Point out each malaria parasite.
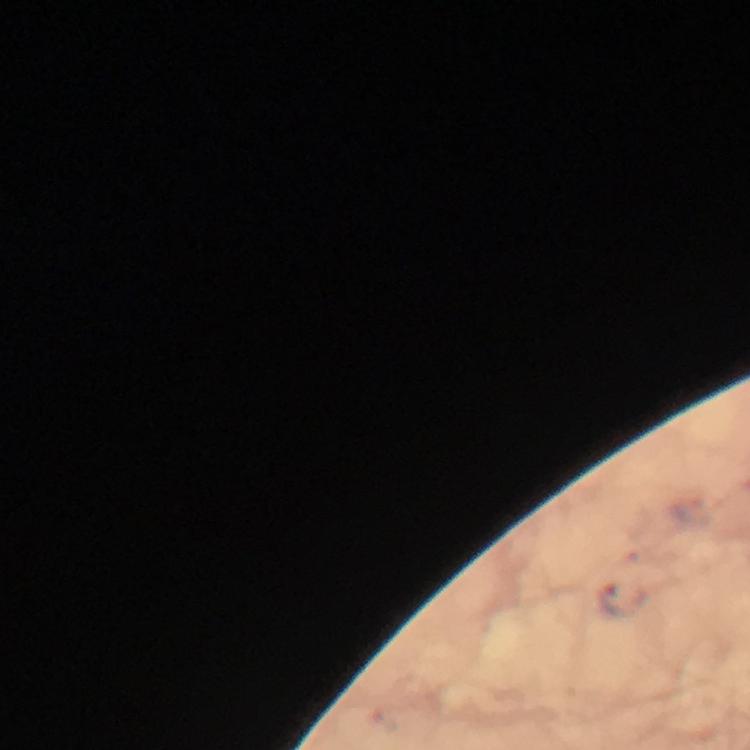

Approximate centers as [x, y] in pixels.
Malaria parasites: [625, 601].

preparation = thick blood film
image size = 750×750 pixels
magnification = 100x
stain = Giemsa
immersion oil = used
context = from a diagnostic examination for malaria
capture = smartphone mounted on the microscope
cropped from = one field of view